Describe the morphology of the erythrocytes.
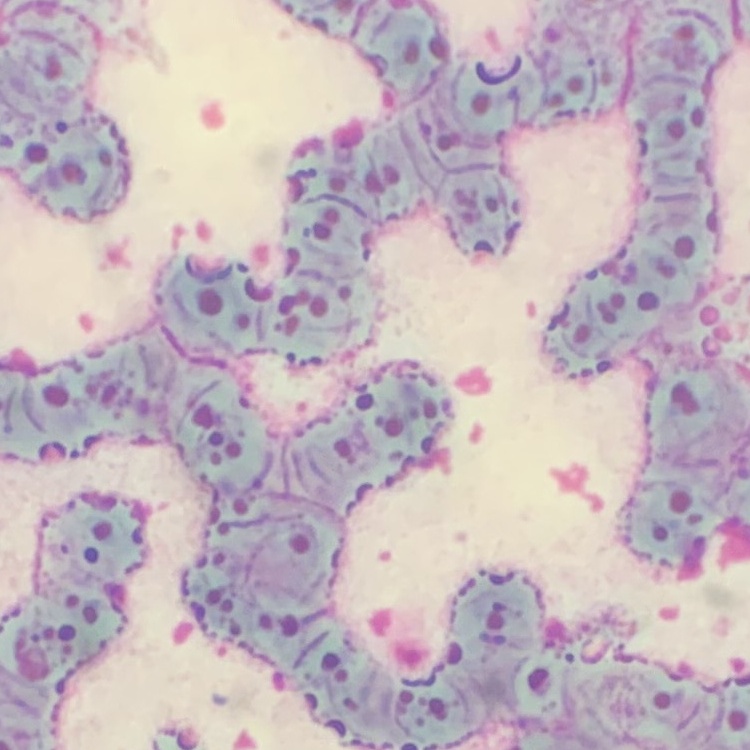

Rouleaux formation.

{
  "stain": "Field's or Giemsa",
  "preparation": "thin peripheral smear",
  "image_type": "one tile cut from a larger photomicrograph"
}